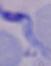

A trypanosome is seen. Micrograph. Captured at 1000x magnification.